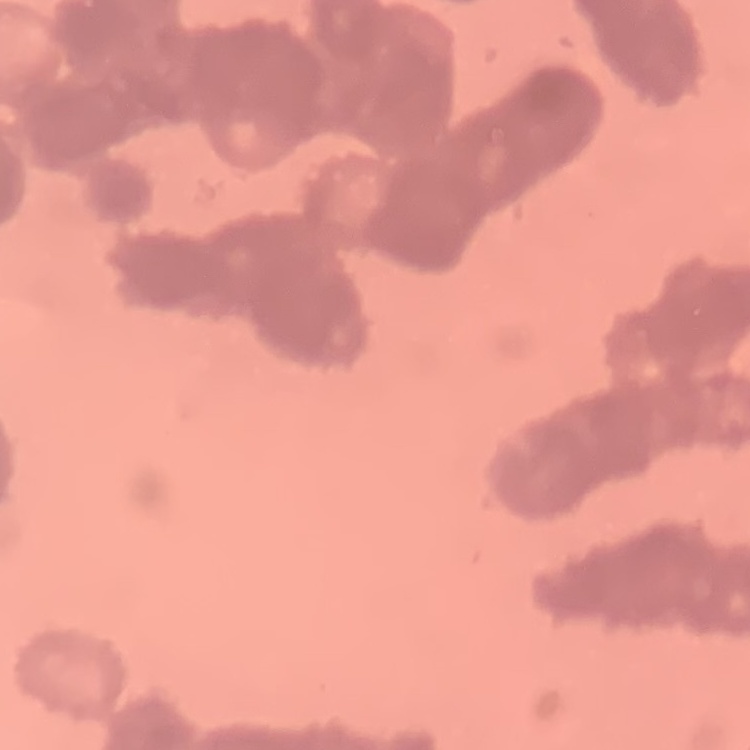

red blood cell morphology = rouleaux formation
preparation = thin blood film
stain = Field's or Giemsa
image type = square crop of a larger photomicrograph